Outline each Plasmodium vivax-infected red blood cell.
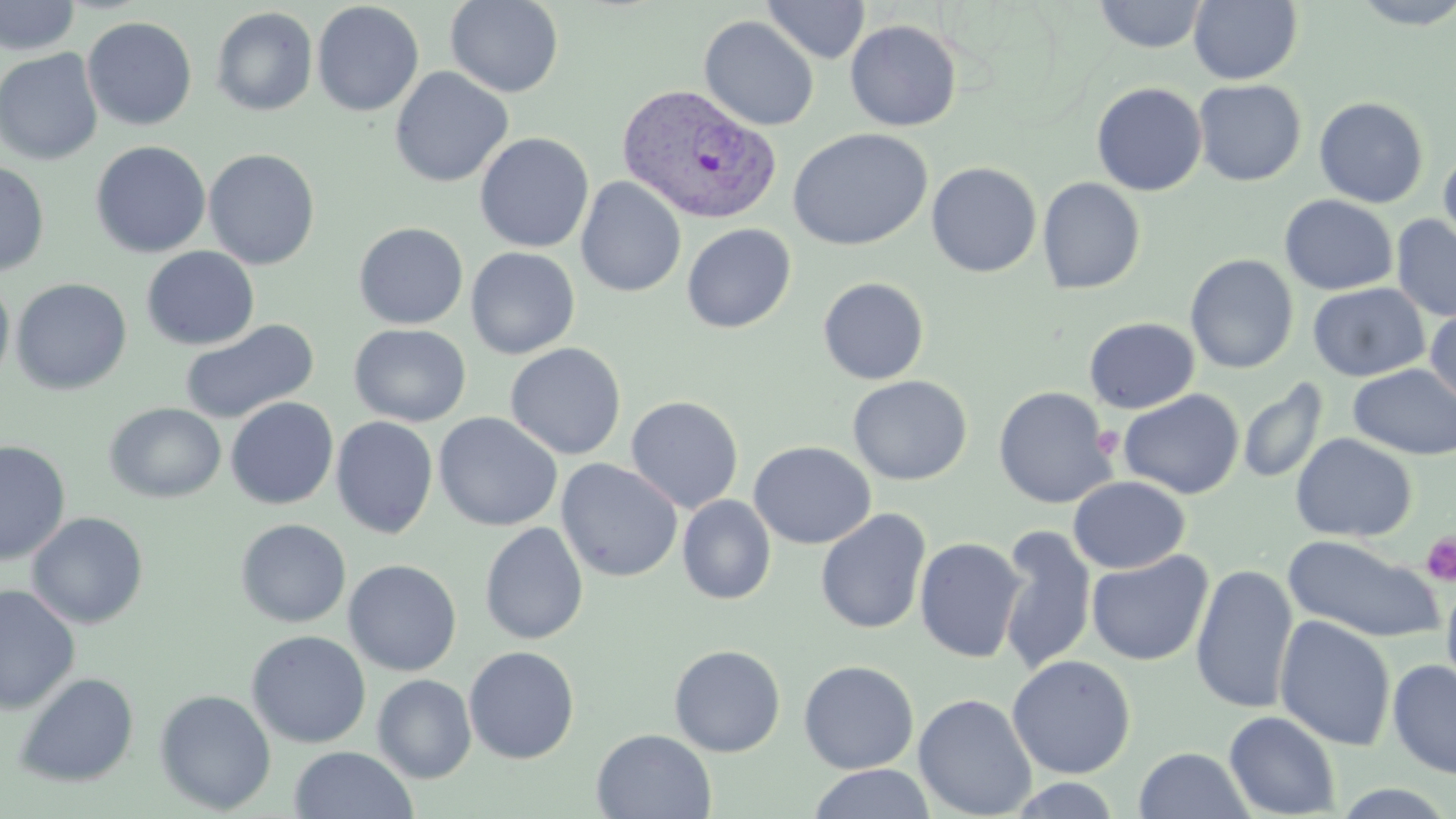

Approximate bounding boxes as (x1,y1)-(x2,y2) corner pairs in pixels.
Plasmodium vivax-infected red blood cells: (616,83)-(780,224).

Uninfected red blood cell locations: (0,0)-(80,56), (445,0)-(564,97), (762,0)-(870,63), (1093,0)-(1208,53), (1188,0)-(1303,85), (1347,0)-(1456,29), (311,2)-(425,117), (210,6)-(318,116), (82,16)-(198,131), (699,16)-(820,131), (845,20)-(962,131), (0,48)-(104,165), (389,67)-(513,188), (1192,79)-(1306,186), (1091,82)-(1207,196), (1314,96)-(1429,208), (788,128)-(933,250), (474,132)-(594,253), (91,140)-(211,258), (1438,147)-(1456,258), (203,148)-(320,270), (0,160)-(50,277), (926,162)-(1042,278), (575,177)-(687,297), (1037,177)-(1145,294), (1279,194)-(1397,295), (1391,214)-(1456,322), (353,222)-(468,329), (681,223)-(796,333), (141,246)-(259,350), (465,247)-(581,360), (1185,254)-(1299,374), (0,276)-(15,389), (11,277)-(132,395), (817,277)-(930,385), (1307,283)-(1430,382), (1425,306)-(1456,410), (1083,317)-(1200,414), (180,319)-(318,424), (348,323)-(471,427), (505,342)-(627,460), (1347,364)-(1456,460), (847,375)-(973,485), (1237,377)-(1329,485), (992,386)-(1117,509), (1118,389)-(1244,499), (625,395)-(744,513), (225,397)-(339,510), (104,402)-(226,503), (433,412)-(563,532), (331,415)-(439,539), (1290,433)-(1418,543), (0,440)-(71,564), (748,440)-(876,549), (556,458)-(683,583), (1068,475)-(1190,574), (677,494)-(776,605), (815,508)-(931,635), (26,512)-(149,629), (236,518)-(351,627), (479,522)-(588,645), (997,525)-(1097,676), (1283,536)-(1445,643), (914,537)-(1027,663), (1087,550)-(1213,666), (343,559)-(462,676), (1190,563)-(1299,715), (1441,573)-(1456,696), (0,584)-(80,715), (1274,615)-(1396,751), (246,630)-(371,748), (668,644)-(786,757), (463,645)-(580,764), (1007,654)-(1136,779), (798,659)-(919,774), (1388,659)-(1456,779), (14,672)-(139,787), (372,674)-(476,782), (154,689)-(276,814), (914,692)-(1037,818), (1224,710)-(1340,818), (592,728)-(717,819), (290,746)-(418,819), (1133,747)-(1253,819), (808,763)-(935,819), (1005,776)-(1124,818), (1328,784)-(1456,818). Platelet locations: (1091,427)-(1123,458), (1420,532)-(1456,585). Slide-level diagnosis: Plasmodium vivax. 1000x magnification. Thin blood film. One field of a larger specimen. Light microscopy. Image is 1456×819 pixels. May-Grünwald-Giemsa stain.